State which parasite is depicted.
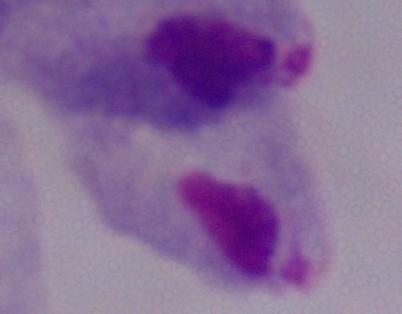

This is a trichomonad.

{
  "modality": "photomicrograph",
  "magnification": "1000x"
}